Assess the morphology of the erythrocytes.
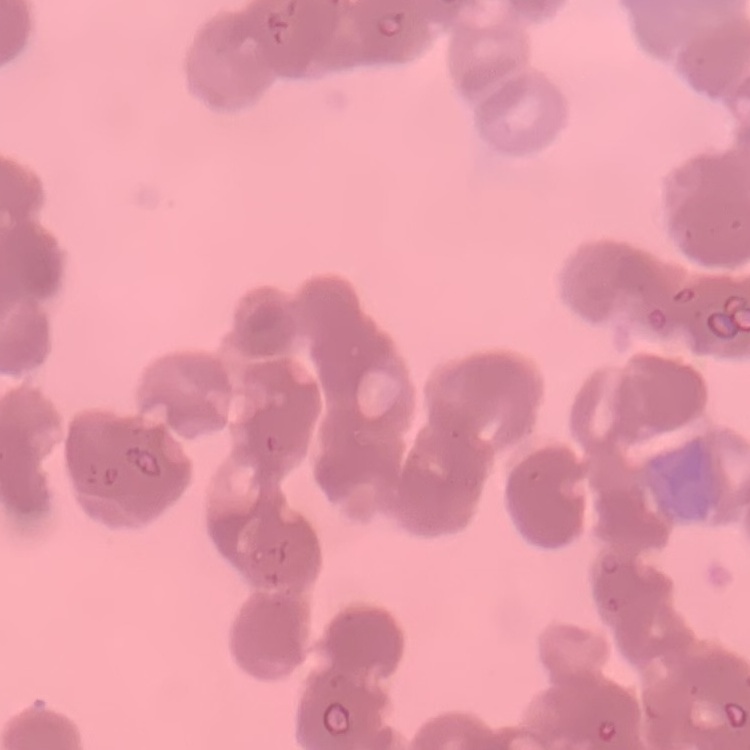

Rouleaux formation.

{
  "image_type": "one tile cut from a larger photomicrograph",
  "preparation": "thin blood smear",
  "stain": "Field's or Giemsa"
}